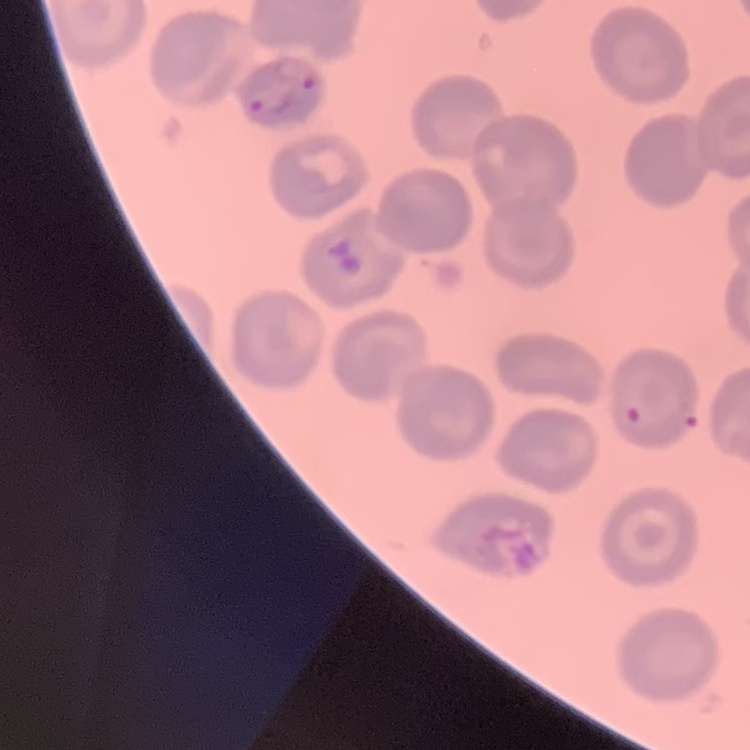 The erythrocytes show no rouleaux formation. Thin blood film. Stained with either Field's or Giemsa. Square crop of a larger photomicrograph.